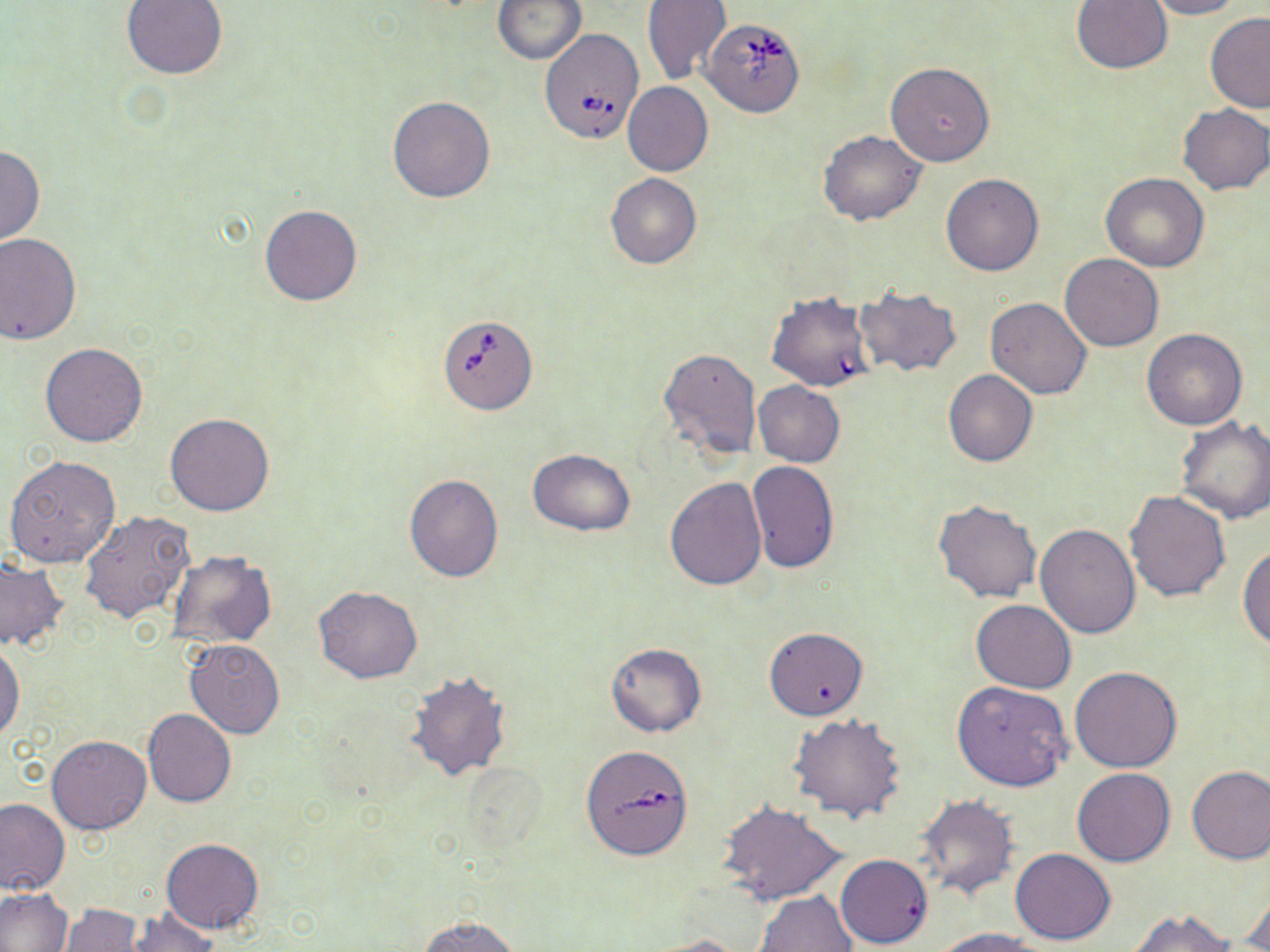
slide_level_diagnosis: Babesia divergens
modality: optical microscopy
image_size: 1270×952 pixels
uninfected_red_blood_cell_locations: 'approximate bounding boxes as named x1/y1/x2/y2 corners in pixels: (x1=121, y1=0, x2=229, y2=79), (x1=492, y1=0, x2=587, y2=64), (x1=1071, y1=0, x2=1173, y2=74), (x1=1145, y1=0, x2=1245, y2=19), (x1=641, y1=1, x2=731, y2=84), (x1=1204, y1=11, x2=1270, y2=116), (x1=884, y1=62, x2=995, y2=166), (x1=622, y1=82, x2=713, y2=177), (x1=387, y1=95, x2=496, y2=202), (x1=1177, y1=104, x2=1270, y2=194), (x1=818, y1=130, x2=926, y2=225), (x1=0, y1=145, x2=44, y2=248), (x1=605, y1=172, x2=701, y2=268), (x1=1100, y1=172, x2=1209, y2=272), (x1=941, y1=174, x2=1043, y2=276), (x1=260, y1=204, x2=363, y2=307), (x1=0, y1=234, x2=81, y2=346), (x1=1060, y1=253, x2=1163, y2=352), (x1=854, y1=287, x2=963, y2=376), (x1=984, y1=296, x2=1091, y2=398), (x1=1141, y1=328, x2=1248, y2=430), (x1=39, y1=342, x2=148, y2=446), (x1=660, y1=348, x2=760, y2=459), (x1=943, y1=368, x2=1037, y2=466), (x1=753, y1=381, x2=844, y2=467), (x1=165, y1=412, x2=275, y2=516), (x1=1176, y1=415, x2=1270, y2=524), (x1=527, y1=449, x2=636, y2=535), (x1=4, y1=454, x2=121, y2=570), (x1=747, y1=459, x2=839, y2=574), (x1=403, y1=475, x2=503, y2=581), (x1=665, y1=476, x2=768, y2=591), (x1=1124, y1=489, x2=1232, y2=602), (x1=933, y1=498, x2=1042, y2=603), (x1=79, y1=511, x2=194, y2=624), (x1=1035, y1=524, x2=1141, y2=638), (x1=1238, y1=542, x2=1270, y2=651), (x1=167, y1=550, x2=276, y2=650), (x1=0, y1=557, x2=68, y2=652), (x1=313, y1=586, x2=423, y2=684), (x1=971, y1=599, x2=1077, y2=692), (x1=763, y1=627, x2=868, y2=719), (x1=0, y1=639, x2=25, y2=742), (x1=186, y1=639, x2=284, y2=739), (x1=605, y1=642, x2=707, y2=737), (x1=1070, y1=667, x2=1182, y2=773), (x1=404, y1=672, x2=513, y2=782), (x1=952, y1=680, x2=1072, y2=792), (x1=142, y1=709, x2=237, y2=807), (x1=788, y1=712, x2=907, y2=824), (x1=46, y1=736, x2=152, y2=835), (x1=1186, y1=765, x2=1270, y2=864), (x1=1073, y1=768, x2=1174, y2=867), (x1=913, y1=795, x2=1018, y2=900), (x1=0, y1=798, x2=69, y2=896), (x1=718, y1=801, x2=848, y2=905), (x1=162, y1=838, x2=262, y2=932), (x1=1010, y1=848, x2=1116, y2=944), (x1=836, y1=853, x2=934, y2=948), (x1=1242, y1=885, x2=1270, y2=951), (x1=0, y1=887, x2=72, y2=952), (x1=754, y1=892, x2=857, y2=952), (x1=60, y1=904, x2=142, y2=952), (x1=127, y1=908, x2=218, y2=952), (x1=1126, y1=908, x2=1237, y2=952), (x1=420, y1=916, x2=521, y2=952), (x1=933, y1=926, x2=1046, y2=952), (x1=640, y1=934, x2=747, y2=952)'
babesia_divergens_infected_red_blood_cell_locations: 'approximate bounding boxes as named x1/y1/x2/y2 corners in pixels: (x1=703, y1=19, x2=802, y2=116), (x1=534, y1=23, x2=649, y2=148), (x1=767, y1=290, x2=874, y2=393), (x1=439, y1=315, x2=538, y2=413), (x1=584, y1=748, x2=690, y2=861)'
stain: May-Grünwald-Giemsa
preparation: thin blood smear
magnification: 1000x
field_of_view: single